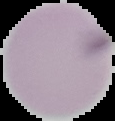

Image is 115×121 pixels. Malaria status: uninfected. Cell region segmented out of the field of view; the surrounding area is masked to black. From a thin blood film.